State the blood parasite species.
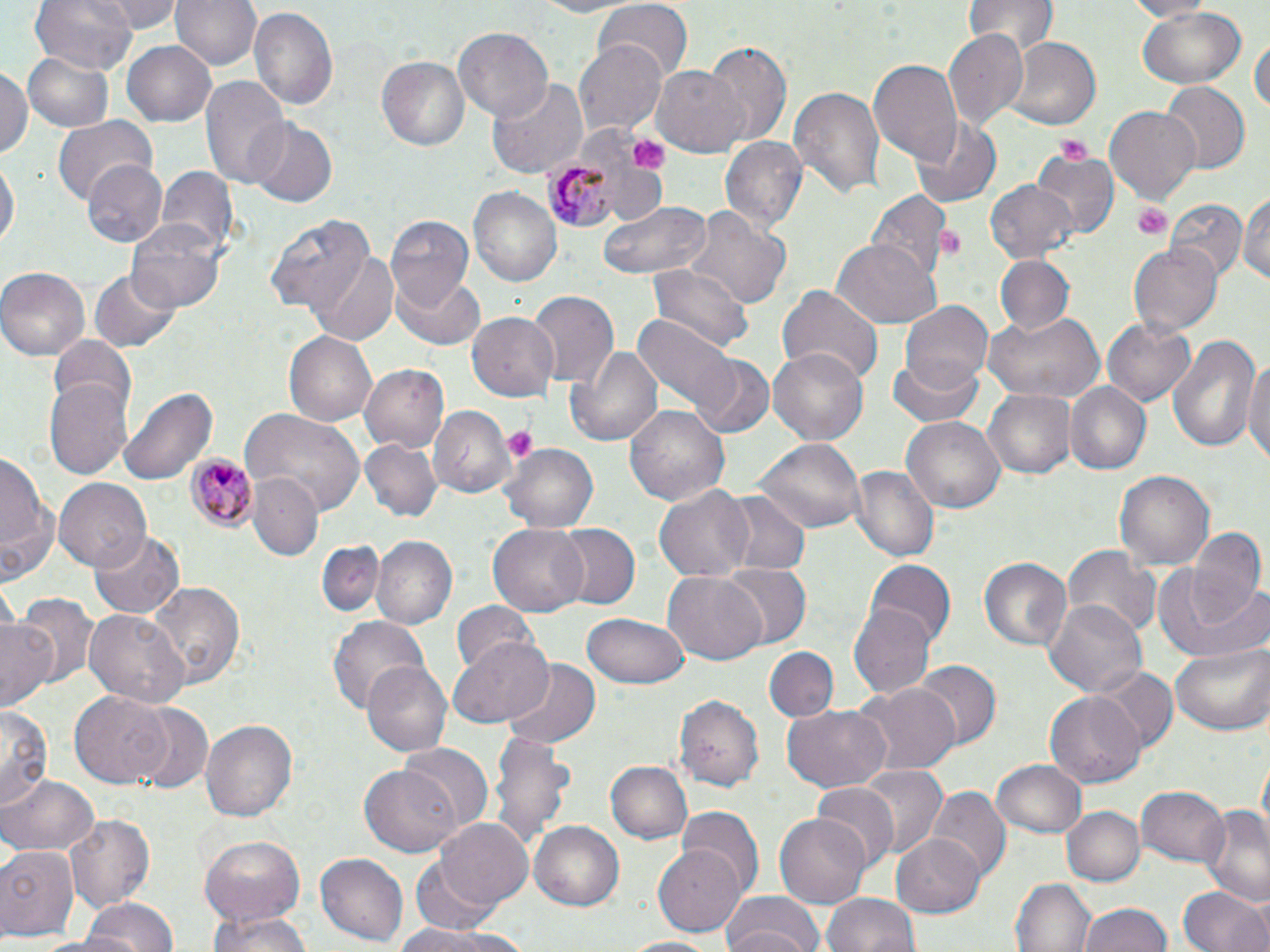

Plasmodium malariae.

{
  "platelet_locations": "approximate bounding boxes as named x1/y1/x2/y2 corners in pixels: (x1=1052, y1=133, x2=1095, y2=163), (x1=624, y1=134, x2=668, y2=172), (x1=1131, y1=202, x2=1171, y2=238), (x1=934, y1=226, x2=962, y2=257), (x1=502, y1=425, x2=539, y2=462)",
  "plasmodium_malariae_infected_red_blood_cell_locations": "approximate bounding boxes as named x1/y1/x2/y2 corners in pixels: (x1=543, y1=151, x2=624, y2=231), (x1=185, y1=455, x2=259, y2=532)",
  "magnification": "1000x",
  "modality": "light microscopy",
  "preparation": "thin blood film",
  "field_of_view": "one of a larger specimen",
  "stain": "May-Grünwald-Giemsa",
  "uninfected_red_blood_cell_locations": "approximate bounding boxes as named x1/y1/x2/y2 corners in pixels: (x1=31, y1=0, x2=137, y2=70), (x1=105, y1=0, x2=181, y2=33), (x1=170, y1=0, x2=259, y2=72), (x1=521, y1=0, x2=643, y2=18), (x1=1115, y1=0, x2=1217, y2=20), (x1=965, y1=1, x2=1058, y2=55), (x1=593, y1=4, x2=693, y2=82), (x1=248, y1=7, x2=338, y2=113), (x1=1134, y1=7, x2=1250, y2=88), (x1=452, y1=28, x2=552, y2=121), (x1=945, y1=30, x2=1027, y2=127), (x1=1251, y1=35, x2=1268, y2=123), (x1=1006, y1=38, x2=1100, y2=130), (x1=576, y1=39, x2=668, y2=138), (x1=122, y1=40, x2=216, y2=127), (x1=704, y1=41, x2=791, y2=146), (x1=22, y1=49, x2=115, y2=132), (x1=375, y1=55, x2=469, y2=153), (x1=867, y1=58, x2=962, y2=164), (x1=653, y1=66, x2=752, y2=156), (x1=0, y1=67, x2=33, y2=161), (x1=201, y1=74, x2=289, y2=188), (x1=488, y1=76, x2=589, y2=179), (x1=1158, y1=83, x2=1248, y2=173), (x1=787, y1=84, x2=884, y2=202), (x1=1105, y1=106, x2=1199, y2=203), (x1=53, y1=114, x2=155, y2=207), (x1=914, y1=117, x2=1001, y2=207), (x1=247, y1=120, x2=337, y2=206), (x1=722, y1=136, x2=808, y2=235), (x1=1030, y1=150, x2=1116, y2=242), (x1=1, y1=157, x2=17, y2=255), (x1=84, y1=160, x2=168, y2=248), (x1=156, y1=168, x2=237, y2=260), (x1=985, y1=180, x2=1078, y2=263), (x1=468, y1=186, x2=563, y2=288), (x1=872, y1=191, x2=949, y2=282), (x1=1236, y1=193, x2=1269, y2=290), (x1=598, y1=199, x2=711, y2=281), (x1=1167, y1=201, x2=1246, y2=281), (x1=685, y1=207, x2=790, y2=312), (x1=267, y1=211, x2=377, y2=318), (x1=388, y1=216, x2=474, y2=307), (x1=125, y1=217, x2=228, y2=314), (x1=829, y1=240, x2=942, y2=328), (x1=1128, y1=244, x2=1222, y2=336), (x1=308, y1=252, x2=397, y2=344), (x1=995, y1=256, x2=1072, y2=334), (x1=647, y1=263, x2=755, y2=354), (x1=0, y1=266, x2=90, y2=360), (x1=91, y1=268, x2=181, y2=352), (x1=388, y1=272, x2=485, y2=351), (x1=777, y1=284, x2=884, y2=387), (x1=527, y1=289, x2=619, y2=390), (x1=899, y1=300, x2=993, y2=391), (x1=983, y1=310, x2=1105, y2=406), (x1=468, y1=313, x2=561, y2=403), (x1=633, y1=314, x2=740, y2=417), (x1=1102, y1=317, x2=1197, y2=406), (x1=284, y1=330, x2=378, y2=425), (x1=1167, y1=331, x2=1259, y2=457), (x1=47, y1=337, x2=136, y2=416), (x1=565, y1=345, x2=662, y2=446), (x1=768, y1=345, x2=867, y2=442), (x1=1245, y1=350, x2=1270, y2=473), (x1=888, y1=354, x2=987, y2=429), (x1=693, y1=355, x2=773, y2=436), (x1=358, y1=364, x2=449, y2=453), (x1=43, y1=373, x2=134, y2=480), (x1=1067, y1=384, x2=1151, y2=474), (x1=117, y1=386, x2=217, y2=487), (x1=984, y1=389, x2=1074, y2=479), (x1=625, y1=405, x2=729, y2=510), (x1=428, y1=408, x2=515, y2=500), (x1=243, y1=410, x2=366, y2=513), (x1=901, y1=418, x2=1006, y2=513), (x1=754, y1=438, x2=867, y2=534), (x1=360, y1=440, x2=443, y2=525), (x1=501, y1=444, x2=597, y2=535), (x1=0, y1=446, x2=55, y2=580), (x1=852, y1=464, x2=940, y2=565), (x1=1116, y1=471, x2=1214, y2=572), (x1=250, y1=475, x2=322, y2=561), (x1=53, y1=479, x2=153, y2=570), (x1=654, y1=485, x2=755, y2=581), (x1=720, y1=489, x2=810, y2=575), (x1=552, y1=523, x2=640, y2=611), (x1=487, y1=524, x2=590, y2=618), (x1=1185, y1=528, x2=1269, y2=624), (x1=90, y1=532, x2=184, y2=618), (x1=372, y1=536, x2=457, y2=630), (x1=318, y1=542, x2=382, y2=618), (x1=1065, y1=544, x2=1160, y2=637), (x1=978, y1=556, x2=1071, y2=652), (x1=867, y1=558, x2=954, y2=648), (x1=720, y1=564, x2=810, y2=648), (x1=1166, y1=568, x2=1270, y2=665), (x1=662, y1=573, x2=767, y2=662), (x1=147, y1=579, x2=247, y2=689), (x1=13, y1=595, x2=100, y2=697), (x1=1044, y1=600, x2=1147, y2=699), (x1=453, y1=601, x2=541, y2=678), (x1=852, y1=602, x2=936, y2=697), (x1=85, y1=609, x2=190, y2=708), (x1=581, y1=614, x2=690, y2=689), (x1=0, y1=616, x2=58, y2=714), (x1=328, y1=616, x2=430, y2=716), (x1=450, y1=636, x2=553, y2=726), (x1=1170, y1=644, x2=1270, y2=736), (x1=764, y1=646, x2=838, y2=722), (x1=501, y1=659, x2=600, y2=748), (x1=361, y1=661, x2=451, y2=760), (x1=913, y1=662, x2=1000, y2=750), (x1=1093, y1=666, x2=1179, y2=755), (x1=857, y1=684, x2=959, y2=776), (x1=71, y1=691, x2=171, y2=787), (x1=1045, y1=691, x2=1147, y2=787), (x1=675, y1=694, x2=765, y2=791), (x1=1, y1=706, x2=53, y2=812), (x1=125, y1=706, x2=212, y2=794), (x1=782, y1=706, x2=889, y2=791), (x1=200, y1=718, x2=298, y2=824), (x1=491, y1=729, x2=574, y2=851), (x1=398, y1=742, x2=493, y2=836), (x1=993, y1=759, x2=1086, y2=839), (x1=605, y1=760, x2=693, y2=845), (x1=360, y1=764, x2=462, y2=857), (x1=853, y1=766, x2=947, y2=862), (x1=2, y1=774, x2=97, y2=857), (x1=810, y1=784, x2=898, y2=872), (x1=1137, y1=785, x2=1228, y2=868), (x1=927, y1=788, x2=1009, y2=882), (x1=1062, y1=805, x2=1144, y2=887), (x1=1201, y1=805, x2=1270, y2=907), (x1=774, y1=808, x2=873, y2=909), (x1=678, y1=809, x2=764, y2=900), (x1=65, y1=814, x2=154, y2=915), (x1=433, y1=818, x2=535, y2=915), (x1=530, y1=822, x2=625, y2=911), (x1=893, y1=831, x2=985, y2=917), (x1=197, y1=835, x2=307, y2=929), (x1=0, y1=844, x2=79, y2=939), (x1=653, y1=846, x2=746, y2=936), (x1=315, y1=853, x2=409, y2=944), (x1=407, y1=858, x2=504, y2=937), (x1=1012, y1=877, x2=1096, y2=952), (x1=1179, y1=884, x2=1270, y2=952), (x1=1009, y1=890, x2=1173, y2=948), (x1=821, y1=893, x2=920, y2=952), (x1=719, y1=895, x2=824, y2=952), (x1=76, y1=898, x2=180, y2=952), (x1=1077, y1=902, x2=1175, y2=952), (x1=204, y1=911, x2=319, y2=952), (x1=391, y1=919, x2=523, y2=950), (x1=620, y1=935, x2=722, y2=952)",
  "image_size": "1270×952 pixels"
}